Locate every uninfected red blood cell.
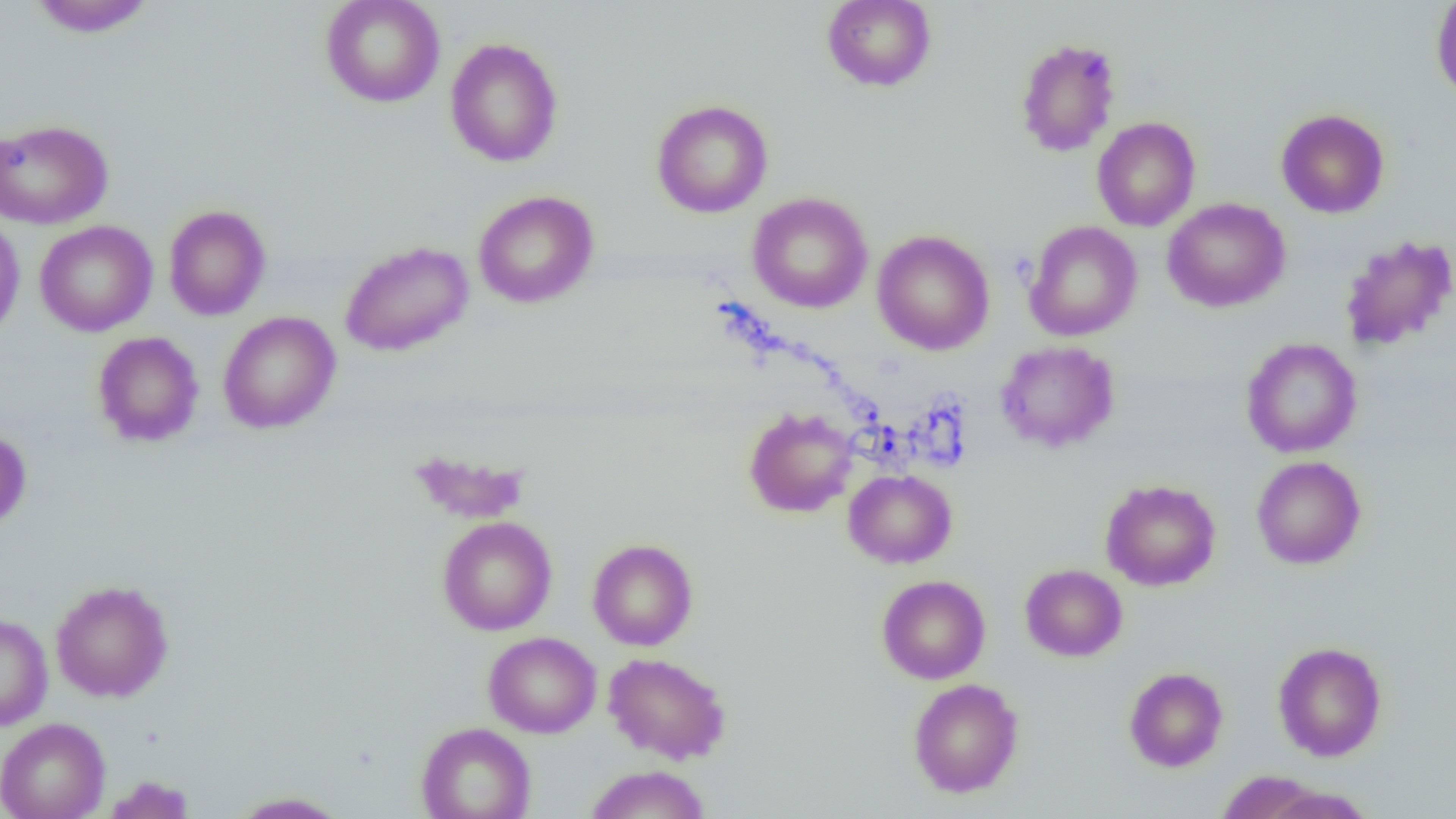
Approximate bounding boxes as (x1, y1, x2, y2) in pixels.
Uninfected red blood cells: (27, 0, 157, 37), (320, 0, 445, 108), (1431, 0, 1456, 102), (822, 1, 937, 91), (444, 37, 563, 167), (1014, 37, 1122, 157), (651, 100, 773, 218), (1276, 109, 1390, 218), (1091, 116, 1201, 231), (0, 118, 114, 230), (473, 190, 599, 308), (747, 192, 873, 313), (1162, 197, 1291, 313), (163, 204, 271, 321), (0, 215, 25, 344), (34, 220, 158, 337), (1024, 221, 1142, 342), (872, 230, 995, 355), (1339, 235, 1456, 351), (339, 240, 474, 356), (217, 311, 341, 434), (92, 331, 205, 447), (1241, 337, 1362, 458), (995, 341, 1120, 452), (744, 408, 858, 517), (0, 427, 31, 532), (408, 450, 532, 524), (1251, 455, 1366, 569), (843, 469, 957, 568), (1101, 479, 1221, 591), (437, 516, 557, 636), (587, 539, 698, 650), (1020, 564, 1127, 662), (877, 575, 990, 684), (50, 580, 173, 702), (0, 612, 53, 730), (483, 632, 601, 738), (1272, 641, 1387, 761), (603, 652, 732, 764), (1124, 666, 1228, 772), (908, 678, 1024, 798), (0, 717, 110, 819), (416, 722, 536, 819), (585, 764, 710, 819), (1215, 770, 1329, 819), (102, 775, 196, 819), (1255, 784, 1378, 819), (229, 791, 350, 818).

Summary:
  - Slide-level diagnosis: negative for blood parasites
  - Magnification: 1000x
  - Preparation: thin blood smear
  - Field of view: one of a larger specimen
  - Modality: optical microscopy
  - Image size: 1456×819 pixels